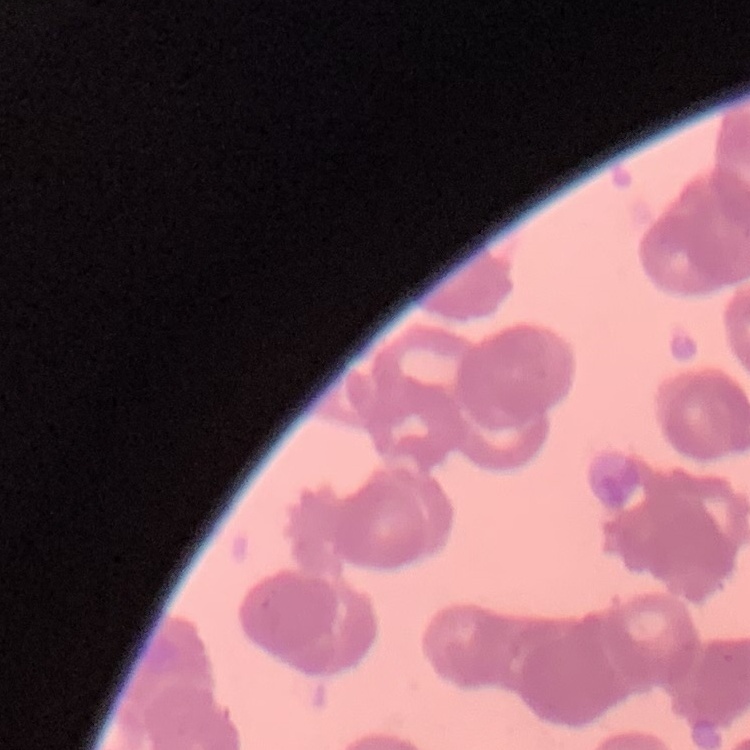
Summary:
  - Red blood cell morphology: rouleaux formation
  - Stain: Field's or Giemsa
  - Preparation: thin blood film
  - Image type: one tile cut from a larger photomicrograph